Name the cell type shown.
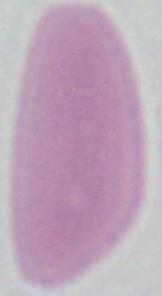
An erythrocyte.

Summary:
  - Modality: photomicrograph
  - Magnification: 1000x